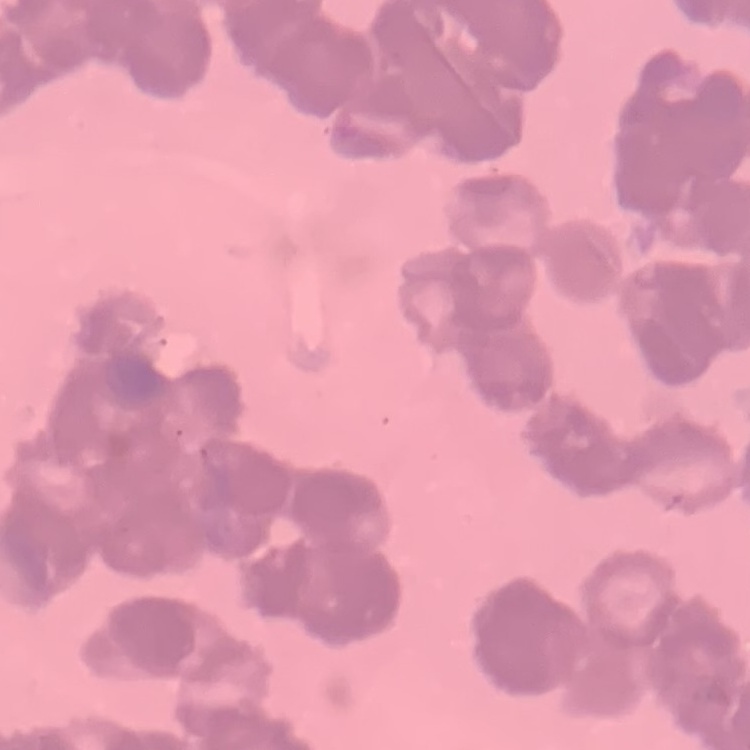
The erythrocytes exhibit rouleaux formation. Stained with either Field's or Giemsa. One tile cut from a larger photomicrograph. Thin peripheral smear.